Name the parasite shown.
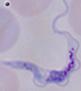
This is a trypanosome.

Captured at 1000x magnification. Photomicrograph.